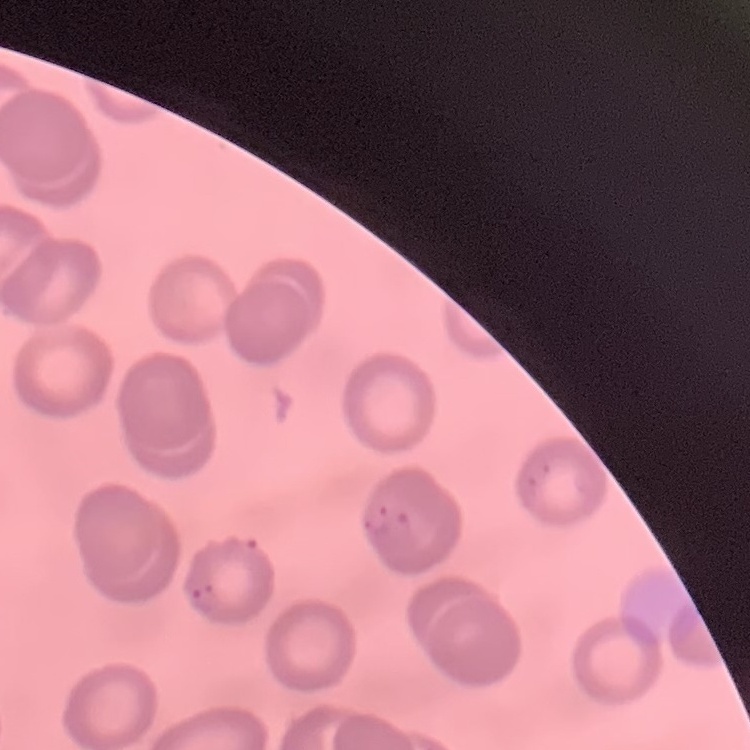
Summary:
  - Erythrocyte morphology: no rouleaux formation
  - Preparation: thin blood film
  - Stain: Field's or Giemsa
  - Image type: one tile cut from a larger photomicrograph